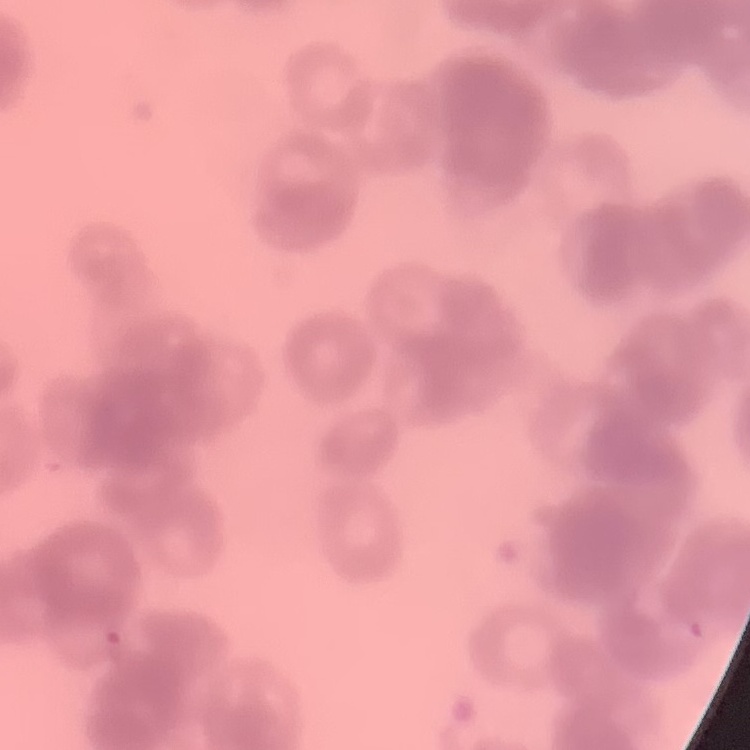

red blood cell morphology = rouleaux formation
stain = Field's or Giemsa
image type = square crop of a larger photomicrograph
preparation = thin blood smear